Classify this cell by malaria status.
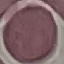
It is uninfected.

Summary:
  - Image type: cell patch, automatically extracted from a larger field of view and resized to 64 × 64 pixels
  - Stain: Giemsa
  - Capture: smartphone camera at the microscope eyepiece
  - Preparation: thin smear